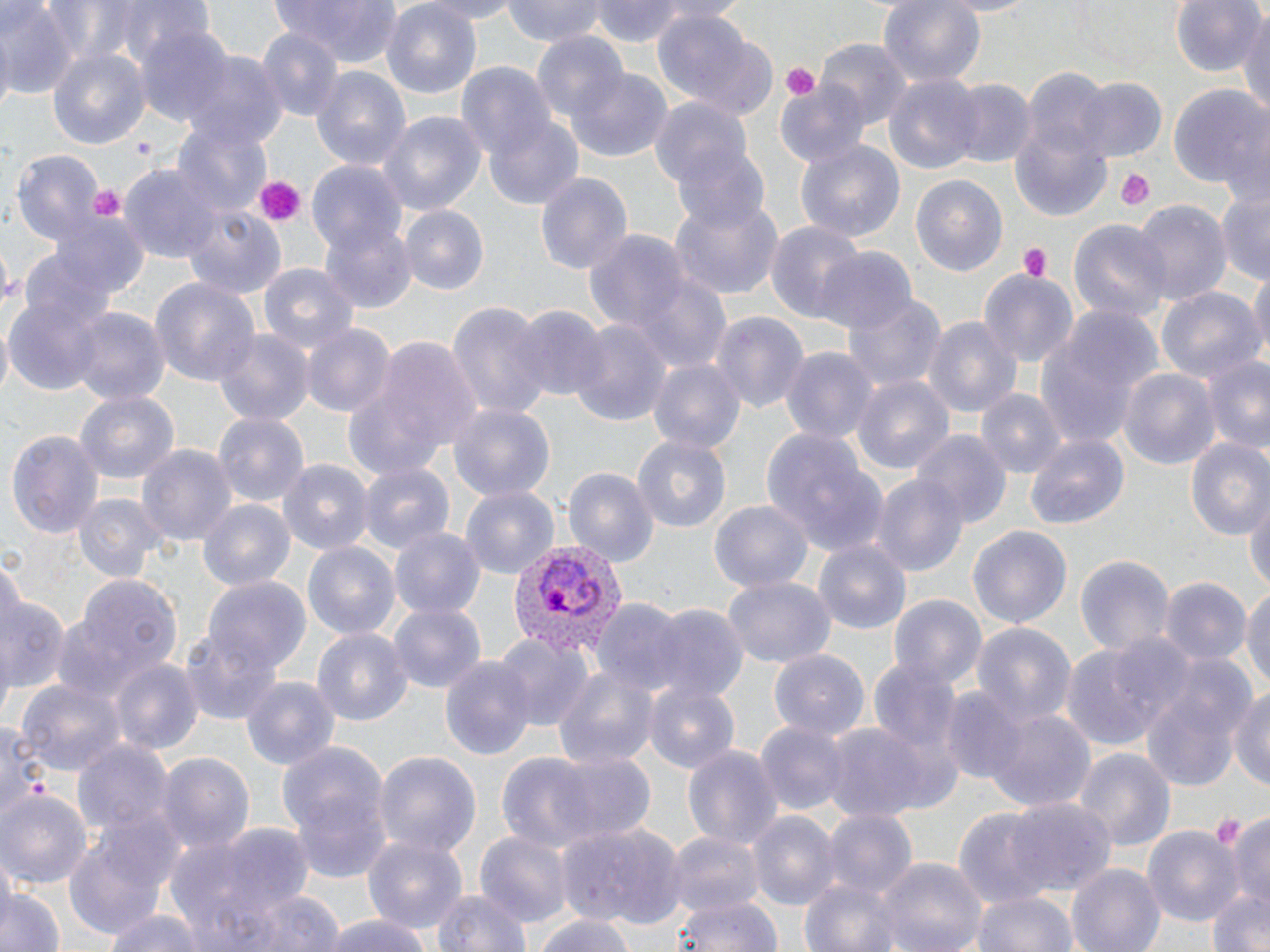
slide-level diagnosis = Plasmodium vivax
uninfected red blood cell locations = approximate bounding boxes as named x1/y1/x2/y2 corners in pixels: (x1=272, y1=0, x2=403, y2=66), (x1=412, y1=0, x2=530, y2=22), (x1=501, y1=0, x2=608, y2=48), (x1=591, y1=0, x2=690, y2=47), (x1=879, y1=0, x2=986, y2=91), (x1=1170, y1=0, x2=1263, y2=78), (x1=85, y1=1, x2=218, y2=71), (x1=381, y1=2, x2=483, y2=98), (x1=0, y1=3, x2=77, y2=98), (x1=1238, y1=12, x2=1270, y2=121), (x1=653, y1=16, x2=778, y2=119), (x1=134, y1=23, x2=235, y2=130), (x1=256, y1=28, x2=343, y2=123), (x1=530, y1=28, x2=629, y2=129), (x1=817, y1=37, x2=910, y2=132), (x1=48, y1=48, x2=150, y2=149), (x1=181, y1=53, x2=288, y2=156), (x1=457, y1=60, x2=559, y2=167), (x1=311, y1=67, x2=413, y2=171), (x1=569, y1=70, x2=672, y2=161), (x1=883, y1=74, x2=982, y2=178), (x1=1072, y1=76, x2=1168, y2=162), (x1=775, y1=79, x2=871, y2=169), (x1=948, y1=79, x2=1035, y2=169), (x1=1168, y1=86, x2=1269, y2=192), (x1=650, y1=94, x2=756, y2=199), (x1=376, y1=108, x2=487, y2=216), (x1=1009, y1=108, x2=1112, y2=222), (x1=484, y1=116, x2=583, y2=209), (x1=173, y1=119, x2=273, y2=221), (x1=795, y1=139, x2=905, y2=243), (x1=670, y1=140, x2=776, y2=235), (x1=11, y1=151, x2=104, y2=249), (x1=122, y1=163, x2=223, y2=265), (x1=306, y1=163, x2=408, y2=262), (x1=536, y1=171, x2=632, y2=276), (x1=911, y1=174, x2=1009, y2=278), (x1=1214, y1=188, x2=1270, y2=286), (x1=667, y1=190, x2=785, y2=300), (x1=1129, y1=198, x2=1231, y2=307), (x1=181, y1=202, x2=284, y2=300), (x1=399, y1=204, x2=488, y2=295), (x1=45, y1=212, x2=148, y2=304), (x1=1068, y1=218, x2=1169, y2=324), (x1=320, y1=219, x2=416, y2=314), (x1=767, y1=221, x2=866, y2=323), (x1=585, y1=227, x2=688, y2=339), (x1=816, y1=246, x2=914, y2=334), (x1=259, y1=263, x2=358, y2=358), (x1=623, y1=266, x2=734, y2=375), (x1=1246, y1=268, x2=1269, y2=367), (x1=977, y1=269, x2=1079, y2=367), (x1=150, y1=278, x2=258, y2=387), (x1=1154, y1=285, x2=1263, y2=389), (x1=5, y1=288, x2=110, y2=398), (x1=843, y1=294, x2=945, y2=396), (x1=448, y1=301, x2=550, y2=423), (x1=513, y1=304, x2=609, y2=403), (x1=69, y1=308, x2=168, y2=410), (x1=1035, y1=310, x2=1159, y2=450), (x1=710, y1=312, x2=808, y2=413), (x1=925, y1=312, x2=1023, y2=420), (x1=566, y1=318, x2=670, y2=429), (x1=299, y1=321, x2=394, y2=417), (x1=212, y1=328, x2=313, y2=428), (x1=358, y1=334, x2=487, y2=473), (x1=780, y1=346, x2=876, y2=446), (x1=1200, y1=352, x2=1270, y2=453), (x1=646, y1=358, x2=746, y2=454), (x1=1118, y1=367, x2=1220, y2=473), (x1=852, y1=375, x2=954, y2=479), (x1=977, y1=388, x2=1065, y2=479), (x1=72, y1=390, x2=181, y2=486), (x1=448, y1=402, x2=556, y2=508), (x1=213, y1=409, x2=310, y2=505), (x1=8, y1=428, x2=103, y2=542), (x1=762, y1=429, x2=885, y2=557), (x1=911, y1=431, x2=1010, y2=527), (x1=1024, y1=431, x2=1129, y2=531), (x1=632, y1=434, x2=733, y2=537), (x1=1184, y1=437, x2=1270, y2=545), (x1=136, y1=443, x2=237, y2=550), (x1=279, y1=458, x2=372, y2=553), (x1=357, y1=461, x2=454, y2=554), (x1=565, y1=466, x2=657, y2=570), (x1=870, y1=475, x2=967, y2=575), (x1=461, y1=485, x2=558, y2=581), (x1=1246, y1=491, x2=1270, y2=595), (x1=73, y1=492, x2=165, y2=583), (x1=198, y1=499, x2=296, y2=593), (x1=710, y1=499, x2=814, y2=595), (x1=968, y1=523, x2=1072, y2=630), (x1=389, y1=526, x2=485, y2=619), (x1=303, y1=540, x2=401, y2=641), (x1=815, y1=541, x2=909, y2=634), (x1=1074, y1=553, x2=1173, y2=658), (x1=73, y1=574, x2=182, y2=682), (x1=204, y1=575, x2=309, y2=675), (x1=1159, y1=576, x2=1250, y2=668), (x1=724, y1=577, x2=836, y2=670), (x1=1244, y1=583, x2=1270, y2=697), (x1=890, y1=593, x2=985, y2=691), (x1=0, y1=597, x2=68, y2=703), (x1=595, y1=599, x2=684, y2=695), (x1=388, y1=601, x2=486, y2=696), (x1=646, y1=602, x2=748, y2=702), (x1=971, y1=620, x2=1076, y2=730), (x1=182, y1=625, x2=282, y2=726), (x1=313, y1=628, x2=412, y2=730), (x1=496, y1=632, x2=592, y2=733), (x1=1057, y1=640, x2=1178, y2=754), (x1=770, y1=648, x2=869, y2=740), (x1=1142, y1=651, x2=1252, y2=788), (x1=442, y1=654, x2=536, y2=763), (x1=107, y1=659, x2=203, y2=757), (x1=869, y1=659, x2=962, y2=761), (x1=552, y1=662, x2=660, y2=769), (x1=241, y1=675, x2=339, y2=773), (x1=15, y1=679, x2=125, y2=780), (x1=641, y1=679, x2=740, y2=777), (x1=1230, y1=682, x2=1270, y2=795), (x1=941, y1=688, x2=1033, y2=785), (x1=982, y1=706, x2=1096, y2=814), (x1=2, y1=720, x2=49, y2=828), (x1=756, y1=720, x2=850, y2=820), (x1=824, y1=722, x2=933, y2=824), (x1=73, y1=741, x2=173, y2=836), (x1=681, y1=743, x2=784, y2=856), (x1=281, y1=745, x2=390, y2=871), (x1=1074, y1=747, x2=1173, y2=854), (x1=375, y1=750, x2=479, y2=860), (x1=156, y1=751, x2=252, y2=857), (x1=492, y1=751, x2=611, y2=860), (x1=540, y1=751, x2=657, y2=849), (x1=0, y1=789, x2=91, y2=886), (x1=1004, y1=799, x2=1117, y2=898), (x1=748, y1=807, x2=837, y2=910), (x1=952, y1=809, x2=1060, y2=906), (x1=821, y1=810, x2=916, y2=900), (x1=1226, y1=812, x2=1270, y2=913), (x1=168, y1=822, x2=315, y2=942), (x1=559, y1=822, x2=686, y2=927), (x1=1144, y1=825, x2=1241, y2=925), (x1=663, y1=829, x2=764, y2=917), (x1=477, y1=832, x2=570, y2=924), (x1=362, y1=833, x2=469, y2=937), (x1=64, y1=837, x2=170, y2=935), (x1=873, y1=857, x2=986, y2=952), (x1=1066, y1=862, x2=1166, y2=952), (x1=797, y1=876, x2=916, y2=952), (x1=1, y1=882, x2=65, y2=952), (x1=1205, y1=886, x2=1270, y2=952), (x1=431, y1=887, x2=532, y2=952), (x1=197, y1=888, x2=350, y2=952), (x1=971, y1=889, x2=1080, y2=952), (x1=668, y1=896, x2=783, y2=952), (x1=102, y1=909, x2=209, y2=952), (x1=531, y1=909, x2=638, y2=952), (x1=316, y1=913, x2=437, y2=952)
field of view = one of a larger specimen
stain = May-Grünwald-Giemsa
preparation = thin blood film
magnification = 1000x
image size = 1270×952 pixels
modality = optical microscopy
platelet locations = approximate bounding boxes as named x1/y1/x2/y2 corners in pixels: (x1=780, y1=62, x2=819, y2=103), (x1=130, y1=135, x2=156, y2=160), (x1=1114, y1=168, x2=1155, y2=212), (x1=252, y1=174, x2=306, y2=228), (x1=88, y1=184, x2=125, y2=222), (x1=1017, y1=243, x2=1053, y2=281)
Plasmodium vivax-infected red blood cell locations = approximate bounding boxes as named x1/y1/x2/y2 corners in pixels: (x1=512, y1=537, x2=626, y2=659)